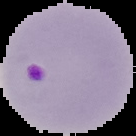
image_type: segmented cell region on a black background
image_size: 136×136 pixels
preparation: thin blood film
result: Plasmodium parasites detected